Classify this cell by malaria status.
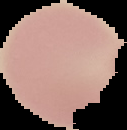
Uninfected.

Summary:
  - Image type: segmented cell region on a black background
  - Image size: 127×130 pixels
  - Preparation: thin blood film